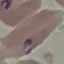

Malaria status: parasitized. Cell patch, automatically extracted from a larger field of view and resized to 64 × 64 pixels. Photographed with a smartphone camera at the microscope eyepiece. Thin blood film. Giemsa stain.